Locate and identify every blood parasite.
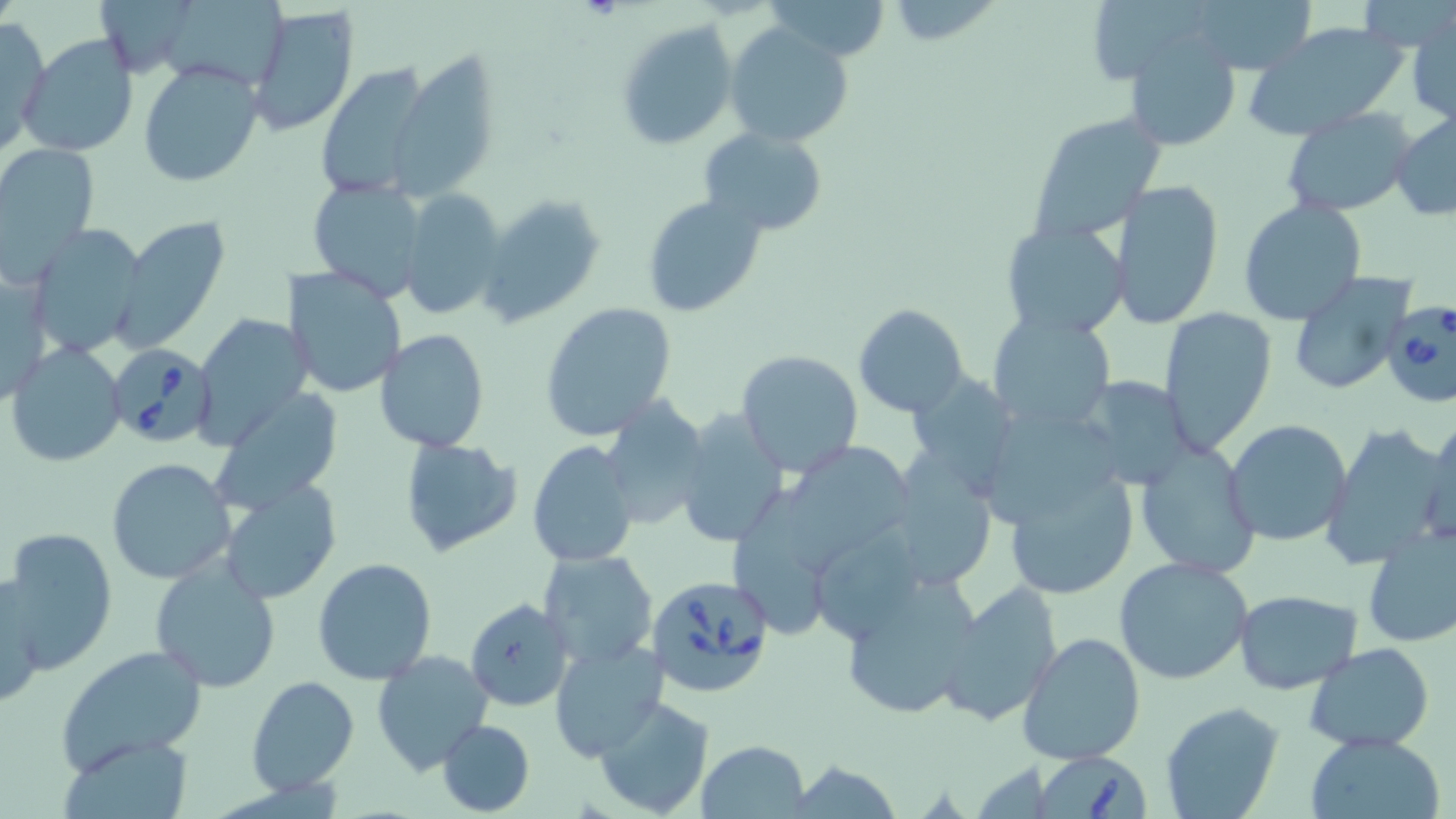
Approximate bounding boxes as (x1, y1, x2, y2) in pixels.
Babesia divergens-infected red blood cells: (1379, 299, 1456, 410), (109, 341, 219, 444), (648, 576, 766, 697), (1034, 747, 1154, 819).
No Plasmodium falciparum, Plasmodium ovale, Plasmodium malariae, Plasmodium vivax, or Trypanosoma brucei observed.

Summary:
  - Uninfected red blood cell locations: (98, 0, 187, 80), (159, 0, 281, 93), (762, 0, 893, 63), (1188, 0, 1317, 76), (886, 2, 998, 46), (247, 6, 360, 137), (1408, 11, 1455, 126), (0, 19, 48, 156), (617, 21, 739, 151), (726, 22, 853, 149), (1242, 22, 1410, 142), (1124, 32, 1244, 154), (18, 34, 139, 157), (395, 49, 500, 196), (138, 59, 262, 189), (313, 61, 433, 197), (1281, 108, 1417, 218), (1027, 110, 1169, 241), (1391, 110, 1456, 221), (699, 127, 828, 236), (0, 142, 100, 279), (1111, 178, 1225, 331), (309, 179, 427, 300), (402, 189, 507, 321), (477, 194, 606, 328), (642, 194, 767, 317), (1238, 198, 1368, 326), (113, 215, 231, 352), (1000, 222, 1131, 338), (30, 224, 149, 358), (284, 266, 409, 399), (1, 268, 50, 408), (1284, 271, 1415, 396), (540, 302, 678, 441), (854, 304, 967, 416), (1158, 306, 1277, 454), (987, 312, 1116, 434), (192, 315, 310, 451), (375, 328, 490, 451), (5, 342, 127, 466), (735, 350, 863, 478), (1072, 378, 1199, 490), (211, 385, 342, 513), (598, 395, 712, 531), (675, 406, 790, 549), (1419, 418, 1456, 549), (1223, 419, 1354, 546), (1318, 420, 1453, 570), (398, 436, 521, 559), (772, 438, 916, 571), (525, 441, 637, 568), (1132, 441, 1262, 580), (105, 457, 238, 586), (883, 458, 999, 593), (1006, 467, 1139, 599), (217, 477, 342, 604), (1358, 523, 1456, 650), (812, 525, 926, 642), (2, 528, 118, 675), (539, 547, 659, 670), (1114, 555, 1257, 685), (148, 556, 281, 692), (311, 557, 438, 683), (836, 571, 983, 722), (0, 576, 45, 709), (937, 581, 1061, 727), (1233, 589, 1361, 693), (465, 598, 573, 711), (1017, 631, 1147, 767), (551, 637, 668, 762), (1305, 642, 1435, 750), (55, 644, 209, 773), (370, 650, 494, 774), (245, 674, 360, 794), (593, 695, 715, 816), (1160, 702, 1285, 819), (437, 718, 535, 816), (60, 731, 195, 818), (1302, 732, 1447, 819), (698, 738, 810, 818), (781, 759, 906, 817)
  - Slide-level diagnosis: Babesia divergens
  - Magnification: 1000x
  - Stain: May-Grünwald-Giemsa
  - Preparation: thin blood smear
  - Modality: light microscopy
  - Image size: 1456×819 pixels
  - Field of view: one of a larger specimen